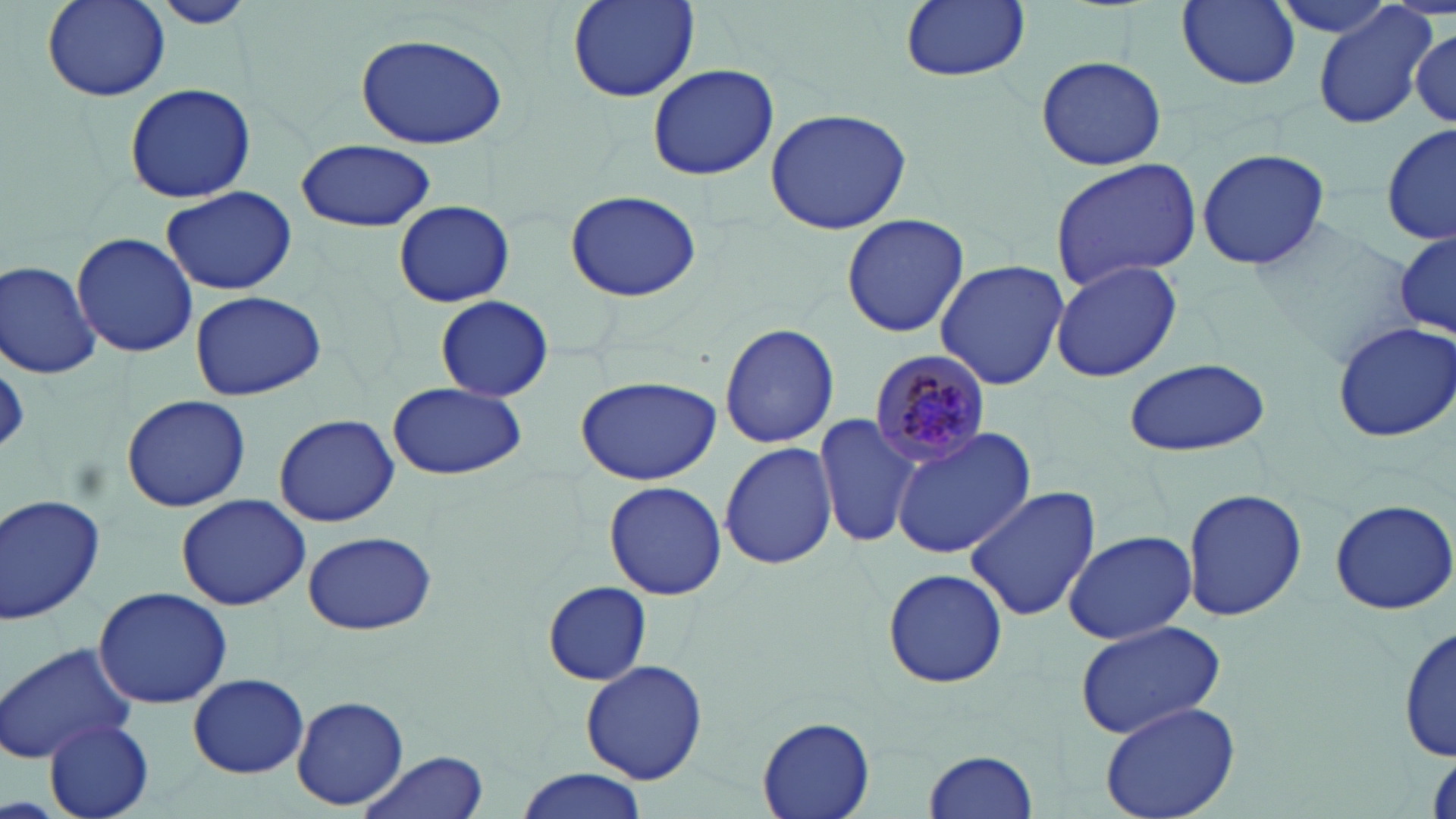
Approximate bounding boxes as (x1,y1)-(x2,y2) corner pairs in pixels. Plasmodium malariae-infected red blood cell locations: (871,353)-(994,468). Uninfected red blood cell locations: (39,0)-(172,103), (156,0)-(253,28), (567,0)-(700,101), (900,0)-(1029,83), (1173,0)-(1307,93), (1264,0)-(1407,40), (1313,5)-(1437,129), (1410,26)-(1454,125), (354,31)-(510,150), (1033,54)-(1166,170), (647,62)-(779,180), (122,83)-(257,203), (765,107)-(913,235), (1382,121)-(1456,247), (296,138)-(437,232), (1194,144)-(1332,271), (1048,158)-(1203,290), (159,186)-(298,296), (564,189)-(700,303), (394,201)-(514,307), (841,213)-(971,338), (1391,225)-(1453,346), (70,232)-(197,358), (934,259)-(1069,392), (1050,259)-(1183,383), (1,261)-(100,379), (188,290)-(328,402), (435,295)-(553,401), (1330,318)-(1456,443), (719,322)-(839,449), (1125,356)-(1272,458), (575,375)-(721,486), (388,381)-(527,481), (121,395)-(252,513), (273,414)-(398,528), (814,415)-(919,548), (891,426)-(1035,560), (717,441)-(837,571), (603,481)-(728,601), (963,486)-(1102,621), (1181,488)-(1307,621), (0,493)-(105,624), (175,494)-(310,610), (1327,498)-(1456,614), (301,531)-(436,635), (1063,531)-(1197,645), (879,568)-(1009,687), (541,581)-(650,684), (95,587)-(231,709), (1074,619)-(1230,739), (1399,623)-(1454,763), (0,640)-(138,766), (580,659)-(708,785), (190,673)-(308,777), (293,696)-(408,810), (1099,699)-(1243,819), (757,714)-(878,819), (45,717)-(154,819), (924,750)-(1040,819), (359,752)-(489,819), (513,767)-(650,819). Slide-level diagnosis: Plasmodium malariae. Light microscopy. May-Grünwald-Giemsa-stained preparation. Captured at 1000x magnification. One field of a larger specimen. Thin blood smear. Image is 1456×819 pixels.